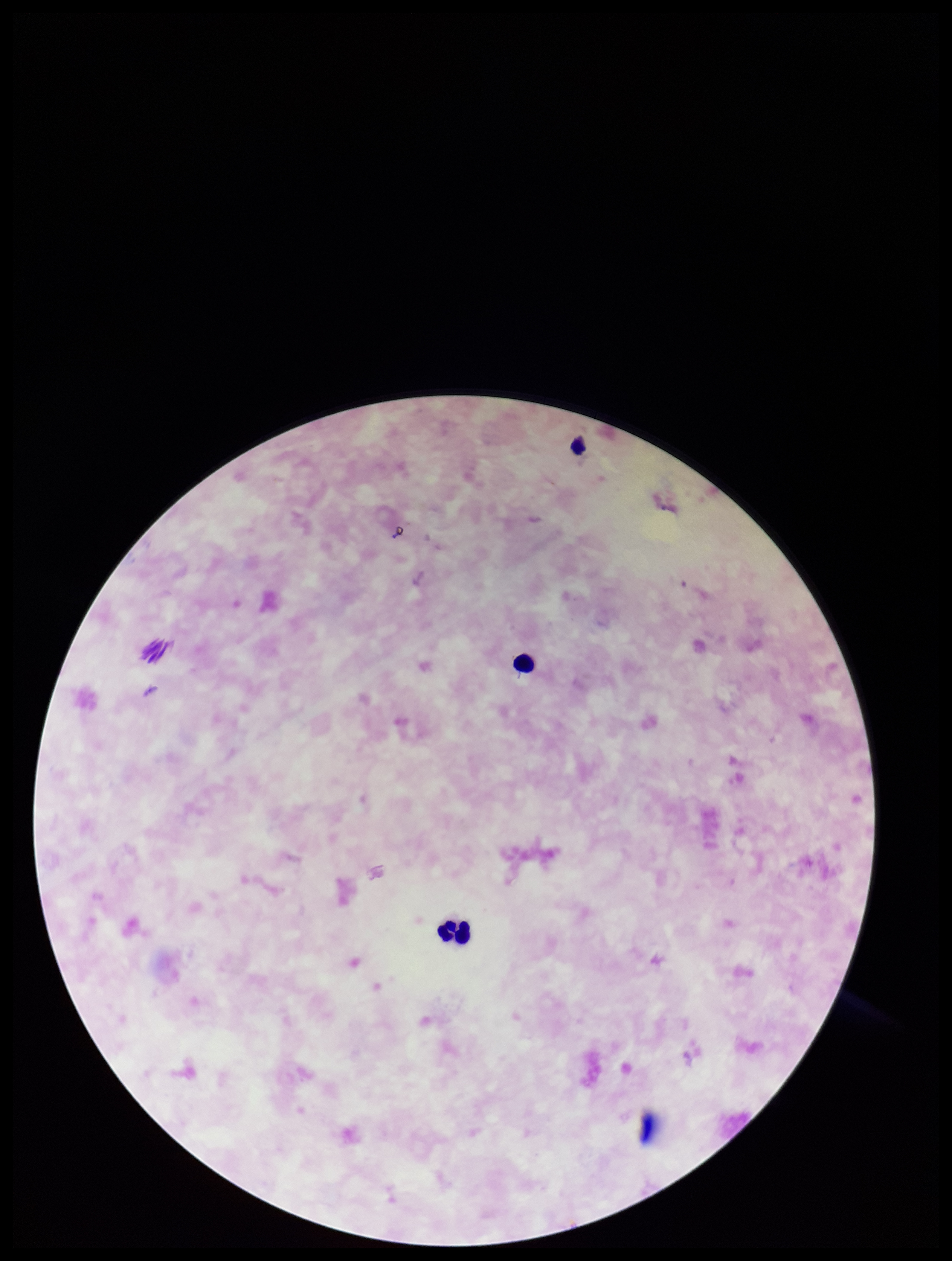

Summary:
  - Image size: 952×1261 pixels
  - Parasite count: 0
  - Plasmodium parasites: none seen
  - Patient malaria status: negative
  - Capture: smartphone photograph through the microscope eyepiece
  - Preparation: thick smear
  - Leukocyte count: 3
  - Stain: Giemsa
  - Field of view: one from this slide